Point out each Plasmodium parasite.
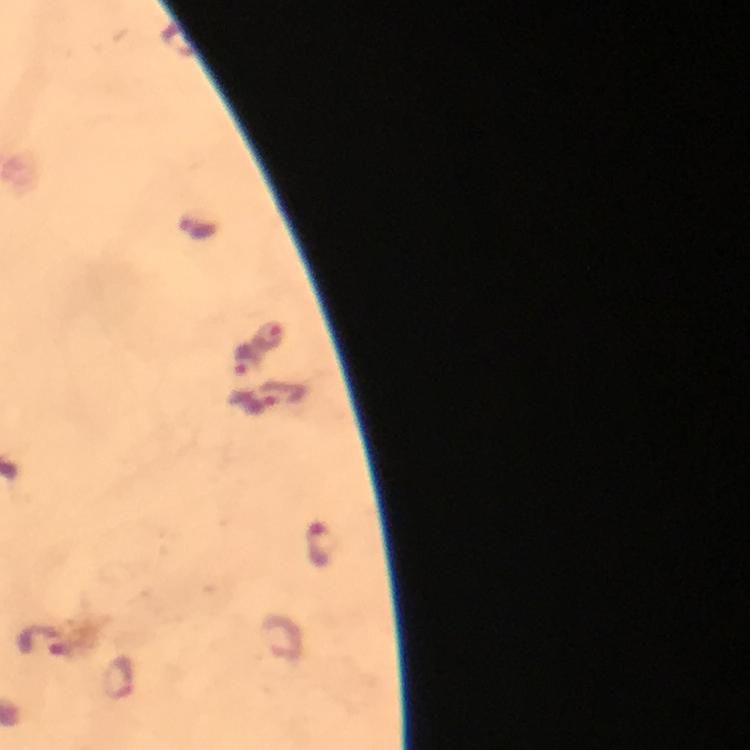
Approximate centers as [x, y] in pixels.
Plasmodium parasites: [270, 337], [245, 360], [282, 395], [320, 544], [284, 636], [120, 678].

capture: smartphone photograph through a microscope
preparation: thick blood smear
immersion_oil: used
stain: Giemsa
magnification: 100x
context: from a diagnostic examination for malaria
cropped_from: a single field of view
image_size: 750×750 pixels